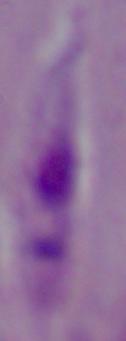
magnification = 1000x
modality = micrograph
identification = Leishmania